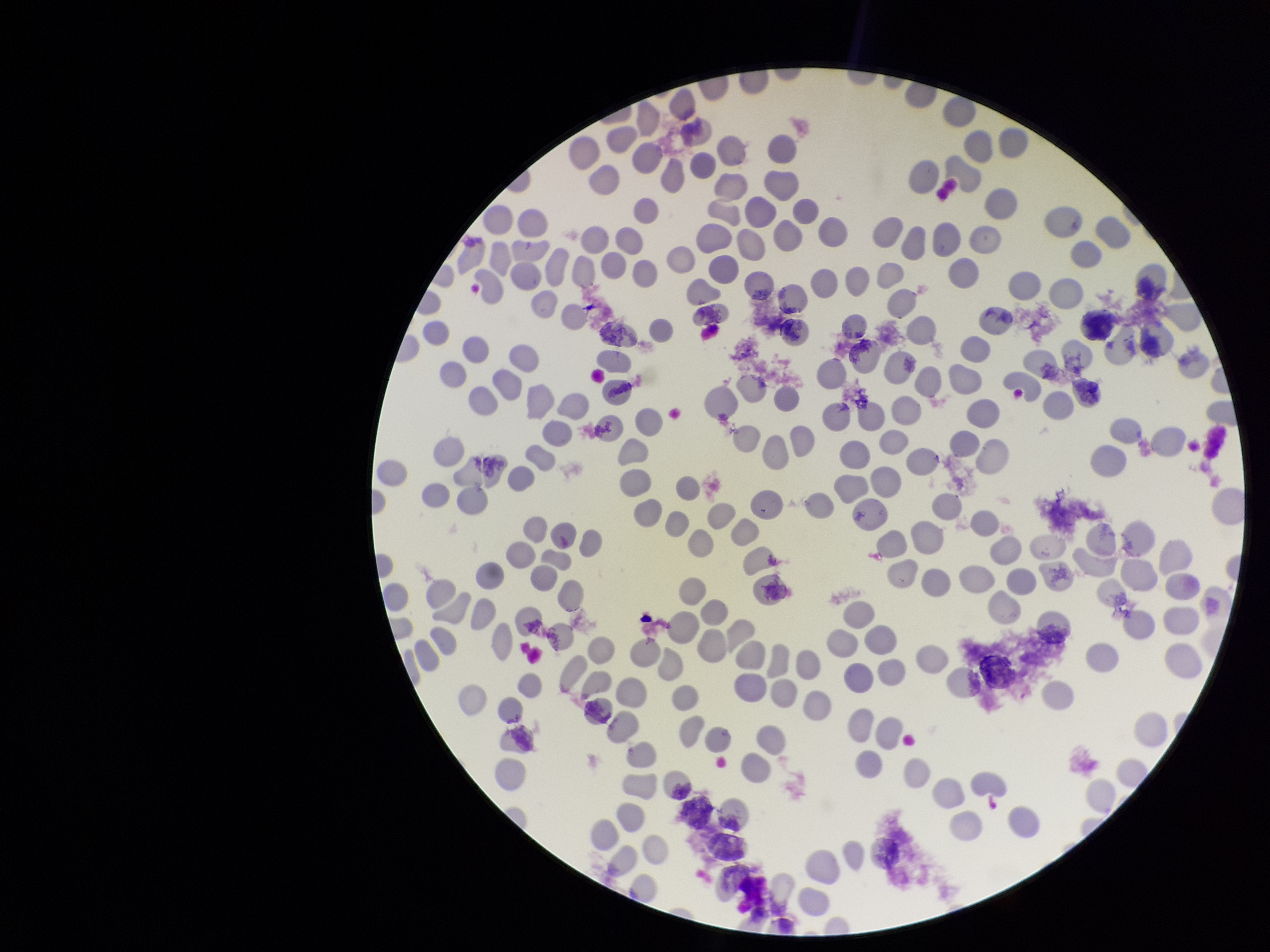 Red blood cell count: 238. Patient malaria status: negative. Preparation: thin smear. Smartphone photograph taken through the eyepiece of a microscope. Parasitized red blood cell count: 0. Image is 1270×952 pixels. Single field of view. Parasitized red blood cells: none seen. Giemsa stain.